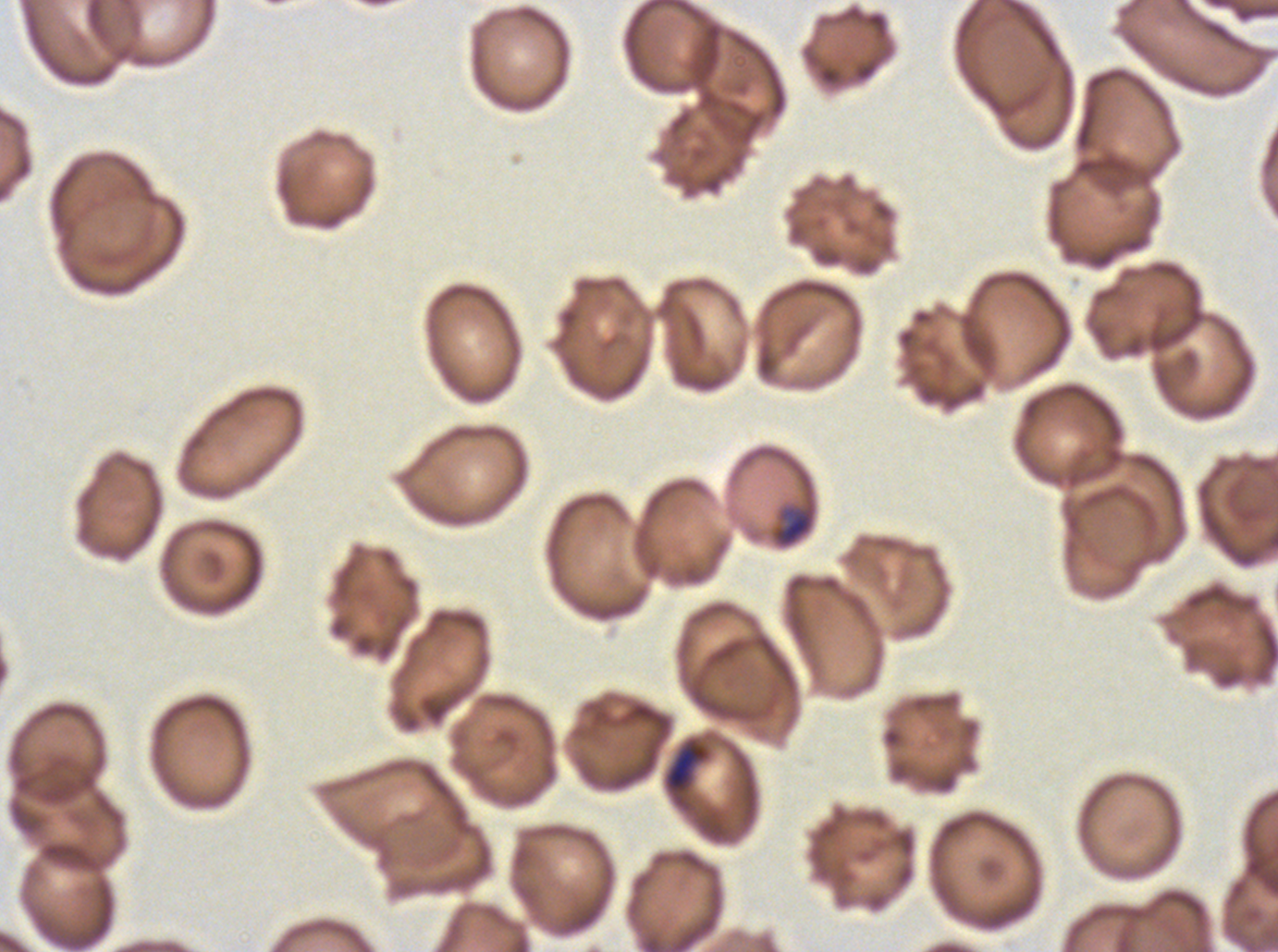

Approximate bounding rectangles given as corner coordinates in pixels from the top-left.
Summary:
  - Mid trophozoite locations: (x1=666, y1=744, x2=707, y2=791)
  - Late-ring/early-trophozoite locations: (x1=771, y1=505, x2=817, y2=548)
  - Stain: Giemsa
  - Image size: 1278×952 pixels
  - Specimen: Plasmodium falciparum from a patient in The Gambia, cultured ex vivo for 24 to 48 hours
  - Field of view: one sub-image of a larger composite
  - Preparation: thin blood film
  - Life-cycle stages observed: late-ring/early-trophozoite, mid trophozoite